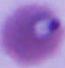

Photomicrograph. A Plasmodium parasite is seen. Captured at either 400x or 1000x magnification.